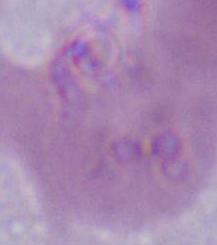

An erythrocyte is shown. Photomicrograph. 1000x magnification.